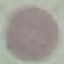
Summary:
  - Malaria status: uninfected
  - Stain: Giemsa
  - Preparation: thin smear
  - Image type: automatically extracted cell patch, resized to 64 × 64 pixels
  - Capture: smartphone camera at the microscope eyepiece